Outline each Plasmodium falciparum-infected red blood cell.
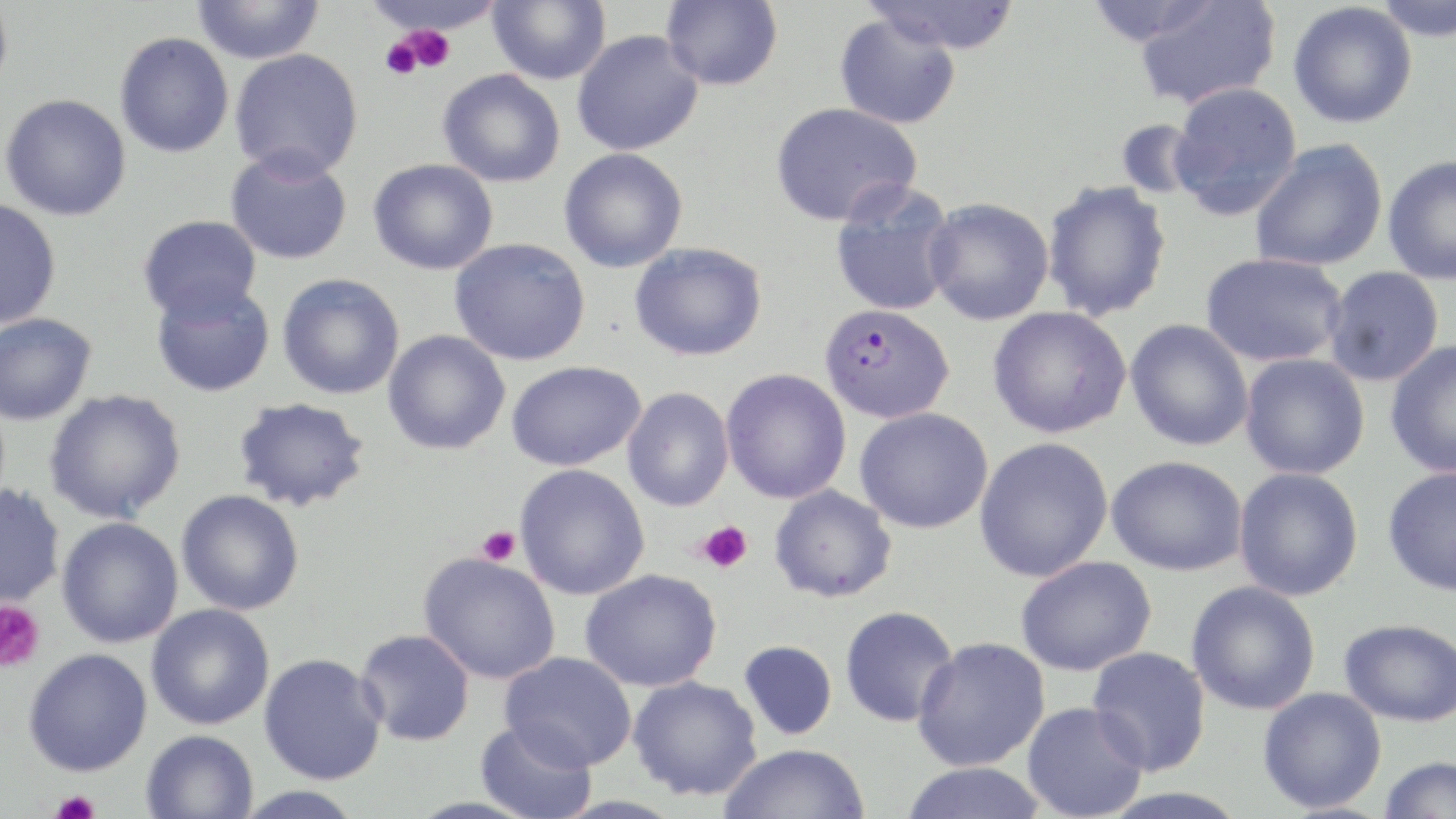

Approximate bounding boxes as (x1, y1, x2, y2) in pixels.
Plasmodium falciparum-infected red blood cells: (819, 303, 954, 423).

slide_level_diagnosis: Plasmodium falciparum
field_of_view: single
modality: light microscopy
preparation: thin blood smear
magnification: 1000x
stain: May-Grünwald-Giemsa
uninfected_red_blood_cell_locations: 'approximate bounding boxes as (x1, y1, x2, y2) in pixels: (0, 0, 13, 100), (191, 0, 325, 64), (488, 0, 611, 86), (661, 0, 783, 90), (861, 0, 1021, 54), (1372, 0, 1455, 44), (1132, 1, 1281, 111), (1288, 2, 1418, 129), (834, 14, 961, 129), (572, 30, 704, 156), (114, 32, 234, 158), (229, 47, 364, 181), (438, 69, 566, 187), (1168, 81, 1303, 219), (1, 94, 131, 221), (769, 102, 922, 227), (1114, 118, 1204, 201), (1249, 140, 1388, 272), (225, 147, 353, 265), (559, 147, 688, 273), (1382, 154, 1456, 285), (368, 158, 498, 275), (830, 180, 961, 317), (1042, 181, 1172, 321), (924, 197, 1054, 325), (0, 199, 61, 329), (138, 214, 262, 322), (449, 237, 590, 365), (629, 242, 768, 361), (1201, 253, 1348, 367), (1323, 265, 1445, 386), (277, 273, 405, 400), (150, 281, 275, 398), (988, 307, 1132, 439), (0, 312, 97, 425), (1125, 319, 1254, 451), (383, 330, 511, 455), (1385, 341, 1456, 479), (1239, 353, 1370, 479), (506, 360, 645, 471), (721, 368, 852, 503), (622, 387, 734, 511), (44, 389, 186, 524), (232, 397, 371, 512), (854, 408, 993, 534), (974, 437, 1113, 582), (1107, 455, 1247, 575), (514, 463, 650, 600), (1382, 466, 1456, 596), (1233, 467, 1364, 601), (0, 483, 65, 609), (769, 484, 897, 603), (176, 489, 305, 615), (57, 517, 184, 648), (418, 552, 561, 684), (1015, 555, 1156, 676), (580, 568, 721, 691), (1186, 581, 1320, 715), (146, 603, 274, 730), (840, 605, 959, 727), (1339, 617, 1456, 727), (356, 628, 475, 747), (912, 637, 1051, 771), (739, 640, 838, 740), (1087, 647, 1211, 775), (23, 648, 152, 776), (499, 651, 637, 771), (259, 653, 387, 785), (628, 675, 763, 801), (1257, 686, 1388, 813), (1022, 701, 1150, 819), (476, 720, 597, 819), (141, 729, 258, 819), (719, 743, 870, 819), (1378, 754, 1455, 818), (900, 761, 1050, 819), (231, 786, 367, 818)'
platelet_locations: 'approximate bounding boxes as (x1, y1, x2, y2) in pixels: (400, 25, 454, 74), (380, 36, 423, 79), (697, 520, 753, 573), (477, 526, 521, 565), (0, 600, 46, 672), (50, 791, 101, 819)'
image_size: 1456×819 pixels